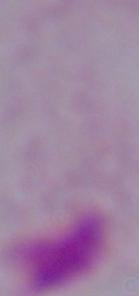

Summary:
  - Magnification: 1000x
  - Identification: trichomonad
  - Modality: photomicrograph